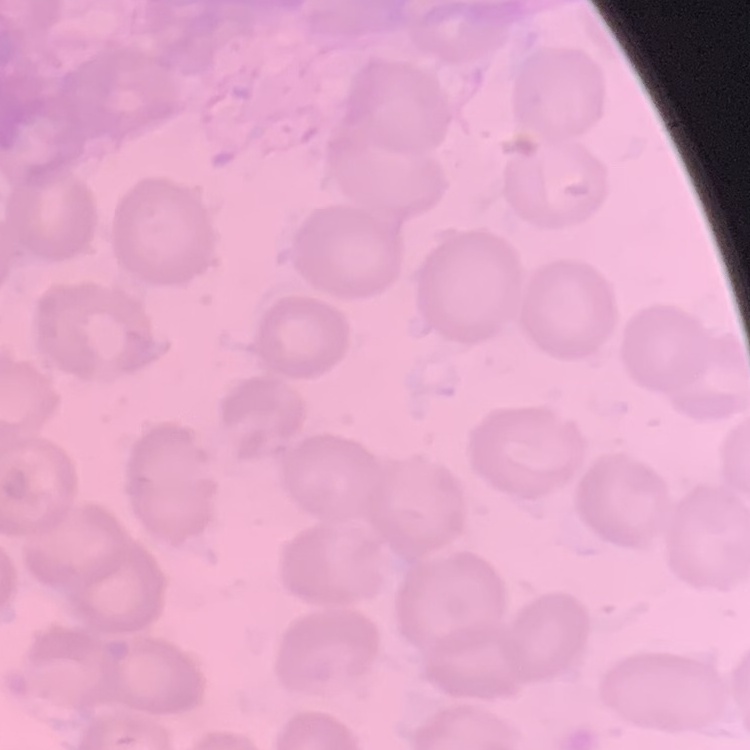

Summary:
  - Erythrocyte morphology: no rouleaux formation
  - Image type: one tile cut from a larger photomicrograph
  - Preparation: thin blood smear
  - Stain: Field's or Giemsa